Assess this cell for malaria.
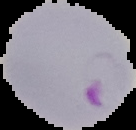
It is parasitized.

From a thin blood film. Image is 136×130 pixels. Cell region segmented out of the field of view; the surrounding area is masked to black.